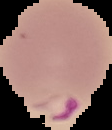
malaria status = parasitized
preparation = thin blood film
image type = cell region segmented out of the field of view; surrounding area masked to black
image size = 112×130 pixels